Assess this cell for malaria.
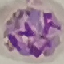

It is parasitized.

Automatically extracted cell patch, resized to 64 × 64 pixels. Photographed with a smartphone camera at the microscope eyepiece. Thin blood smear. Giemsa stain.